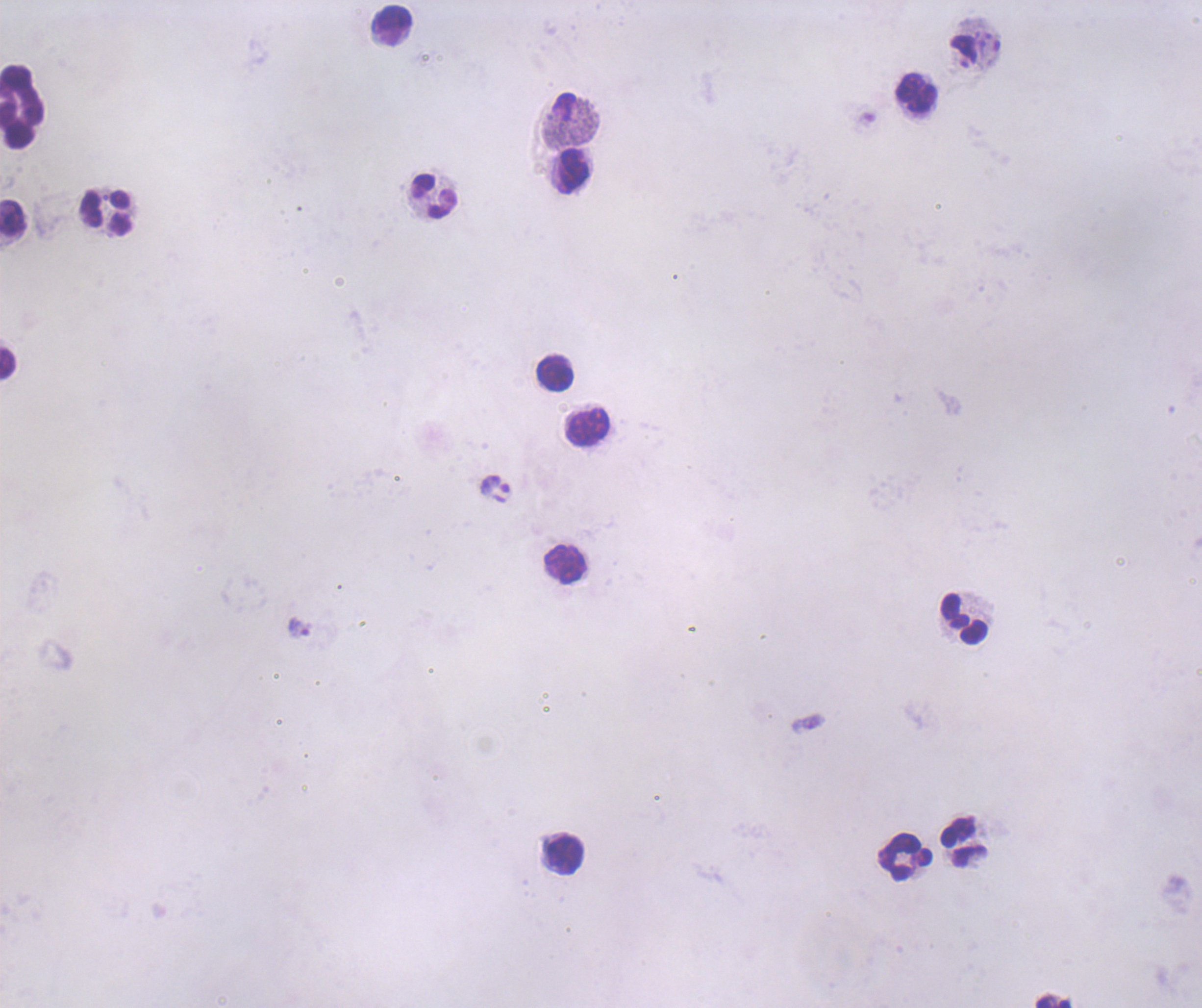
Approximate centers as [x, y] in pixels. Trophozoite locations: [299, 628]. Leukocyte locations: [393, 19], [916, 93], [22, 106], [572, 170], [434, 196], [105, 213], [13, 217], [8, 363], [554, 372], [589, 427], [565, 564], [963, 618], [963, 842], [565, 856], [905, 857], [1053, 1002]. Background quality: poor. Single field of view. Image is 1202×1008 pixels. Thick smear of blood. Previously used in an actual diagnosis. 100x magnification. Romanowsky-stained preparation. Coloration quality: bad. Result: Plasmodium parasites identified.